Report the malaria status of this cell.
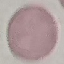

Uninfected.

Acquired by smartphone through the microscope eyepiece. Thin smear of blood. Cell patch, automatically extracted from a larger field of view and resized to 64 × 64 pixels. Giemsa stain.